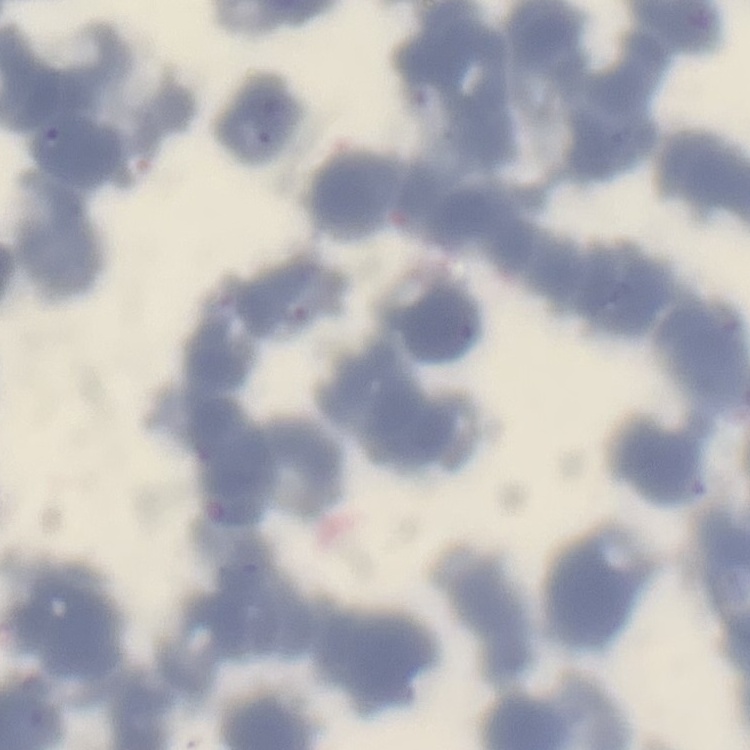
Summary:
  - Red blood cell morphology: rouleaux formation
  - Preparation: thin blood smear
  - Image type: square crop of a larger photomicrograph
  - Stain: Field's or Giemsa